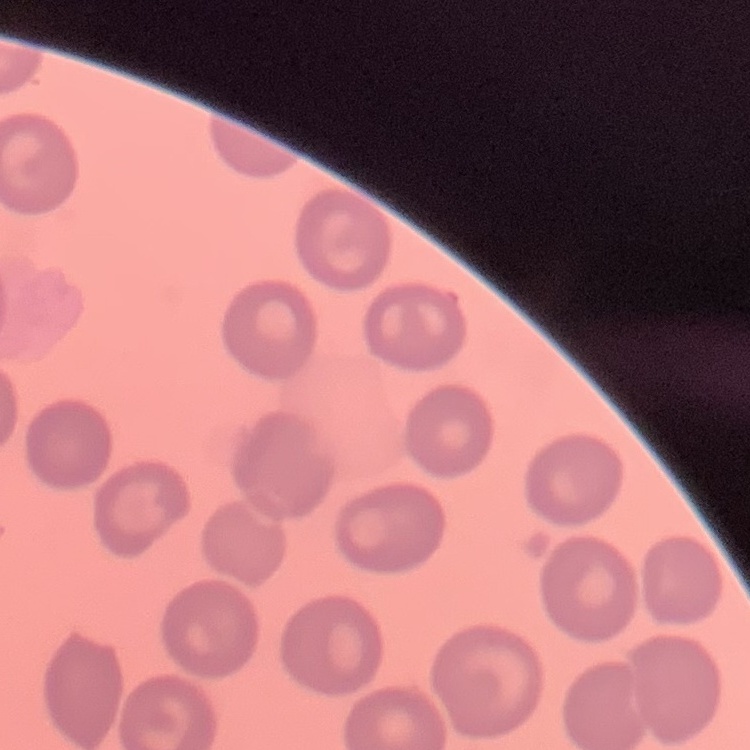

Summary:
  - Erythrocyte morphology: no rouleaux formation
  - Image type: one tile cut from a larger photomicrograph
  - Preparation: thin peripheral smear
  - Stain: Field's or Giemsa